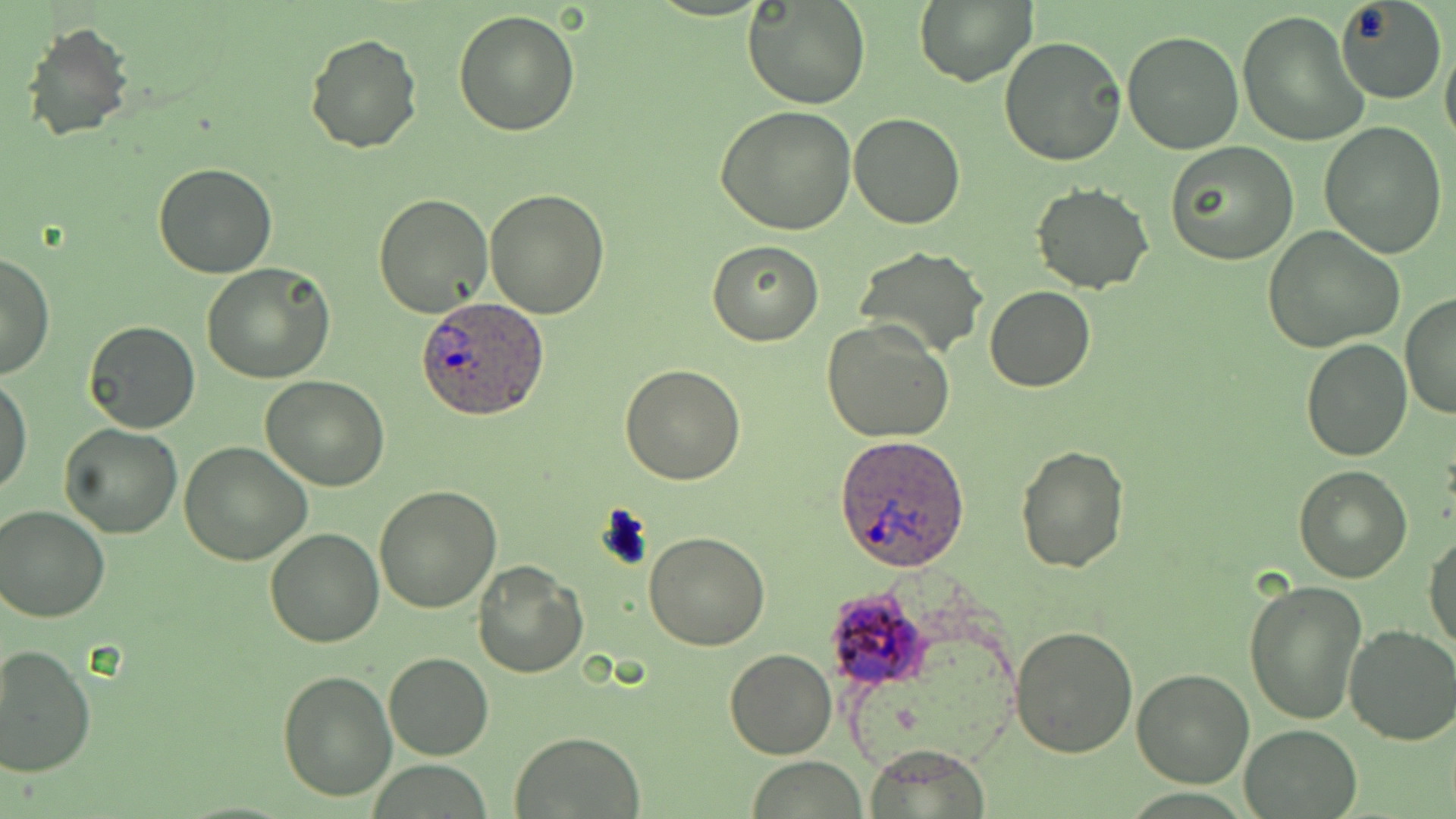 Approximate bounding boxes as named x1/y1/x2/y2 corners in pixels. Plasmodium ovale-infected red blood cell locations: (x1=417, y1=296, x2=550, y2=421), (x1=835, y1=434, x2=970, y2=572), (x1=821, y1=584, x2=933, y2=691). Uninfected red blood cell locations: (x1=744, y1=0, x2=871, y2=110), (x1=914, y1=0, x2=1036, y2=86), (x1=1334, y1=0, x2=1447, y2=104), (x1=1237, y1=9, x2=1368, y2=149), (x1=454, y1=10, x2=579, y2=136), (x1=22, y1=20, x2=135, y2=144), (x1=1121, y1=30, x2=1245, y2=154), (x1=304, y1=32, x2=421, y2=153), (x1=1000, y1=37, x2=1127, y2=167), (x1=1441, y1=39, x2=1456, y2=154), (x1=715, y1=105, x2=857, y2=234), (x1=848, y1=111, x2=965, y2=229), (x1=1321, y1=121, x2=1449, y2=257), (x1=1166, y1=142, x2=1297, y2=264), (x1=151, y1=164, x2=277, y2=279), (x1=1030, y1=184, x2=1154, y2=294), (x1=485, y1=189, x2=611, y2=319), (x1=372, y1=192, x2=492, y2=318), (x1=1263, y1=226, x2=1404, y2=353), (x1=706, y1=240, x2=825, y2=346), (x1=853, y1=246, x2=988, y2=361), (x1=0, y1=251, x2=55, y2=380), (x1=203, y1=263, x2=335, y2=383), (x1=984, y1=286, x2=1096, y2=392), (x1=1399, y1=292, x2=1456, y2=423), (x1=822, y1=319, x2=954, y2=443), (x1=82, y1=322, x2=201, y2=434), (x1=1302, y1=338, x2=1411, y2=461), (x1=620, y1=362, x2=746, y2=484), (x1=0, y1=373, x2=33, y2=497), (x1=260, y1=375, x2=389, y2=491), (x1=58, y1=422, x2=183, y2=539), (x1=179, y1=443, x2=312, y2=566), (x1=1013, y1=444, x2=1130, y2=574), (x1=1294, y1=467, x2=1412, y2=583), (x1=373, y1=486, x2=502, y2=612), (x1=1, y1=504, x2=112, y2=622), (x1=263, y1=526, x2=385, y2=648), (x1=1424, y1=530, x2=1456, y2=652), (x1=644, y1=531, x2=769, y2=650), (x1=473, y1=560, x2=590, y2=677), (x1=1243, y1=578, x2=1368, y2=726), (x1=1343, y1=624, x2=1456, y2=746), (x1=1010, y1=625, x2=1140, y2=757), (x1=0, y1=643, x2=96, y2=777), (x1=725, y1=648, x2=836, y2=761), (x1=383, y1=652, x2=493, y2=761), (x1=277, y1=668, x2=398, y2=802), (x1=1132, y1=668, x2=1255, y2=787), (x1=1240, y1=723, x2=1362, y2=817), (x1=509, y1=733, x2=646, y2=818), (x1=865, y1=744, x2=991, y2=819), (x1=748, y1=758, x2=868, y2=818). Slide-level diagnosis: Plasmodium ovale. Single field of view. Thin blood film. Image is 1456×819 pixels. Captured at 1000x magnification. Optical microscopy. May-Grünwald-Giemsa stain.